Locate every blood parasite and identify its species.
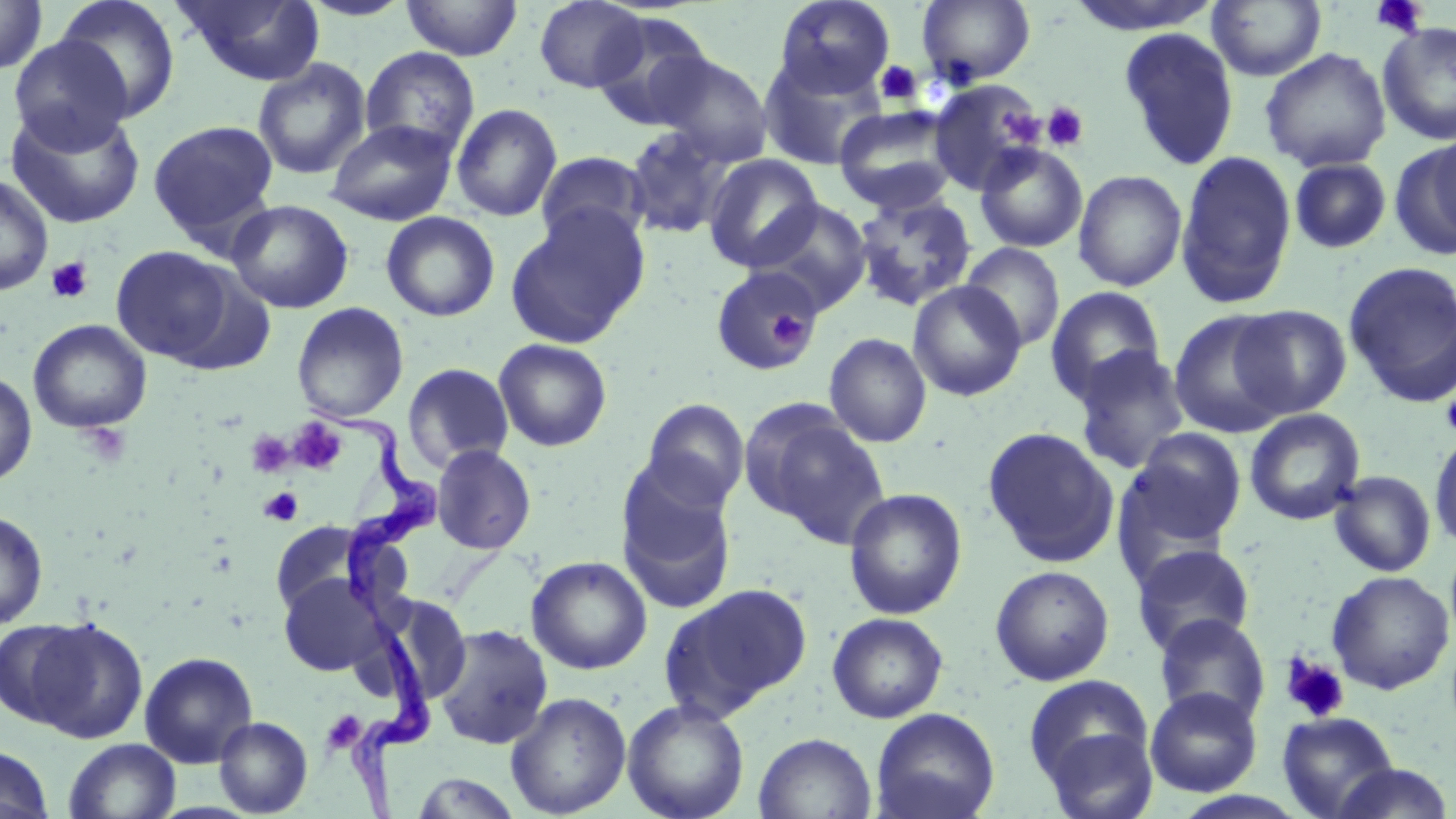
Approximate bounding boxes as (x1,y1)-(x2,y2) corner pairs in pixels.
Trypanosoma brucei: (306,401)-(447,614), (330,609)-(441,818).
No Plasmodium falciparum, Plasmodium ovale, Plasmodium malariae, Plasmodium vivax, or Babesia divergens observed.

Platelet locations: (1370,0)-(1431,38), (875,60)-(924,107), (1042,102)-(1089,151), (997,107)-(1045,148), (46,256)-(94,304), (770,308)-(810,349), (1440,384)-(1456,442), (288,418)-(347,474), (81,425)-(131,467), (246,430)-(294,479), (259,487)-(303,526), (1281,655)-(1349,723), (320,710)-(368,755). Uninfected red blood cell locations: (53,0)-(181,123), (175,0)-(326,85), (299,0)-(417,21), (400,0)-(523,61), (773,0)-(895,98), (917,0)-(1036,86), (1063,0)-(1227,36), (0,1)-(48,75), (534,1)-(648,92), (1207,1)-(1326,81), (591,12)-(718,131), (1377,21)-(1456,145), (1117,28)-(1239,171), (8,35)-(133,151), (359,46)-(480,158), (1260,48)-(1391,172), (652,52)-(774,165), (758,54)-(886,171), (252,58)-(372,180), (929,79)-(1045,195), (4,103)-(147,230), (451,103)-(562,222), (834,106)-(960,215), (325,119)-(459,226), (147,120)-(279,247), (622,126)-(734,239), (654,132)-(803,253), (1395,136)-(1456,259), (974,143)-(1088,252), (535,150)-(651,248), (1176,151)-(1297,309), (704,154)-(823,271), (1289,159)-(1391,253), (1073,170)-(1188,292), (0,173)-(53,295), (852,193)-(978,313), (226,199)-(354,313), (749,200)-(873,313), (504,208)-(650,350), (381,211)-(500,322), (961,242)-(1065,351), (110,245)-(238,365), (1344,261)-(1456,407), (710,265)-(822,374), (908,280)-(1027,402), (1045,286)-(1167,405), (291,303)-(409,423), (1231,305)-(1352,418), (1169,311)-(1291,437), (28,319)-(152,433), (824,332)-(932,448), (493,338)-(612,452), (1073,348)-(1188,474), (402,363)-(514,472), (0,372)-(37,486), (642,399)-(750,509), (744,404)-(889,546), (1244,408)-(1366,525), (982,426)-(1119,568), (1122,428)-(1247,552), (1429,428)-(1456,551), (431,444)-(536,555), (616,468)-(736,613), (1329,471)-(1436,577), (843,488)-(967,620), (0,511)-(49,629), (270,521)-(370,616), (1132,543)-(1255,656), (526,555)-(653,675), (990,565)-(1115,686), (1326,571)-(1455,694), (278,573)-(386,676), (659,582)-(812,722), (827,612)-(948,723), (1154,613)-(1270,726), (21,617)-(148,743), (1,619)-(93,729), (433,624)-(553,749), (139,651)-(258,768), (1024,674)-(1157,806), (1145,687)-(1262,797), (505,692)-(631,818), (622,698)-(750,819), (870,707)-(1000,819), (1277,711)-(1400,819), (214,716)-(313,817), (753,732)-(876,819), (64,738)-(181,819), (0,745)-(55,819), (1327,762)-(1455,819), (411,771)-(524,818), (1170,791)-(1314,819). Slide-level diagnosis: Trypanosoma brucei. Light microscopy. Image is 1456×819 pixels. Thin blood film. 1000x magnification. One field of a larger specimen. May-Grünwald-Giemsa-stained preparation.